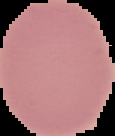 The area outside the segmented cell region is set to black. Result: negative for malaria parasites. Image is 115×136 pixels. From a thin blood film.